Report the malaria status of this cell.
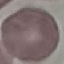
It is uninfected.

Acquired by smartphone through the microscope eyepiece. Automatically extracted cell patch, resized to 64 × 64 pixels. Thin blood film. Giemsa stain.